Name the blood parasite species.
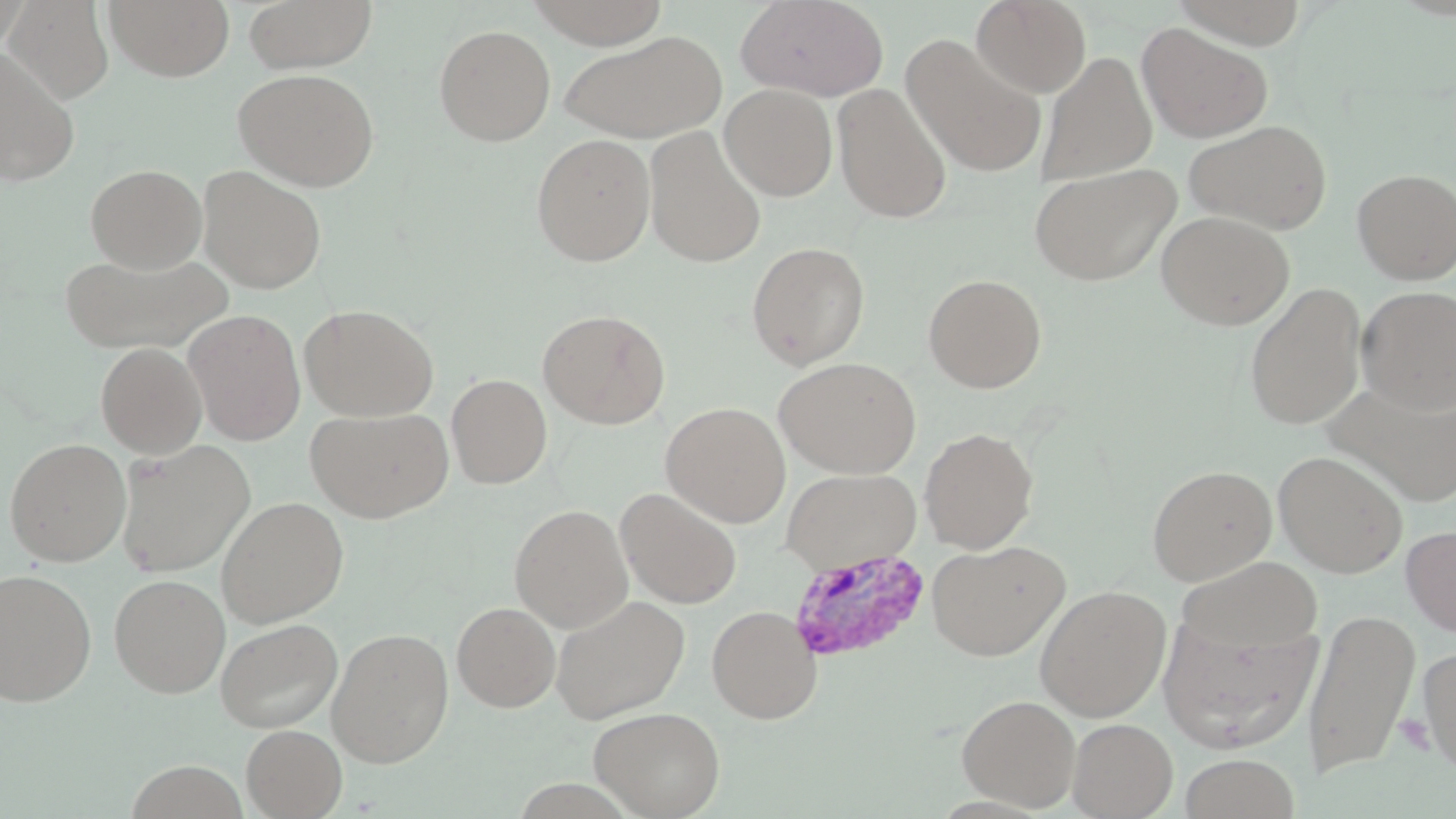

Plasmodium vivax.

image size = 1456×819 pixels
magnification = 1000x
preparation = thin blood film
Plasmodium vivax-infected red blood cell locations = approximate bounding boxes as [x1, y1, x2, y2] in pixels: [786, 546, 929, 663]
modality = optical microscopy
uninfected red blood cell locations = approximate bounding boxes as [x1, y1, x2, y2] in pixels: [3, 0, 114, 105], [105, 0, 235, 82], [241, 0, 378, 72], [524, 0, 671, 49], [735, 0, 889, 101], [971, 0, 1092, 97], [1169, 0, 1310, 48], [1137, 22, 1273, 143], [433, 24, 556, 146], [559, 29, 727, 143], [901, 34, 1047, 178], [0, 46, 79, 187], [1037, 51, 1157, 185], [233, 68, 380, 191], [719, 83, 838, 200], [831, 84, 952, 223], [1184, 119, 1332, 234], [644, 126, 766, 268], [531, 133, 656, 266], [1029, 163, 1181, 286], [85, 164, 207, 273], [197, 165, 327, 294], [1352, 168, 1456, 284], [1157, 210, 1295, 330], [746, 241, 870, 370], [59, 249, 229, 357], [922, 273, 1047, 393], [1244, 282, 1367, 430], [1357, 286, 1456, 414], [300, 304, 438, 422], [537, 308, 670, 428], [184, 309, 306, 445], [96, 342, 207, 458], [774, 356, 922, 478], [446, 373, 552, 489], [1328, 378, 1456, 506], [661, 402, 791, 526], [306, 406, 454, 523], [919, 427, 1039, 553], [3, 438, 131, 566], [115, 439, 255, 578], [1273, 450, 1408, 577], [1147, 464, 1277, 585], [781, 467, 921, 573], [615, 486, 743, 609], [216, 495, 349, 627], [509, 504, 633, 632], [1401, 524, 1456, 636], [927, 539, 1070, 661], [1176, 556, 1324, 654], [0, 567, 97, 706], [109, 573, 230, 697], [1035, 585, 1171, 721], [550, 594, 691, 724], [452, 601, 561, 712], [707, 605, 821, 723], [1302, 608, 1419, 779], [1157, 616, 1322, 752], [214, 617, 343, 734], [327, 627, 454, 767], [1418, 647, 1456, 774], [956, 693, 1081, 811], [588, 705, 726, 818], [1067, 718, 1177, 818], [241, 724, 347, 818], [1179, 753, 1302, 818]
platelet locations = approximate bounding boxes as [x1, y1, x2, y2] in pixels: [1395, 714, 1434, 753]
field of view = one of a larger specimen
stain = May-Grünwald-Giemsa